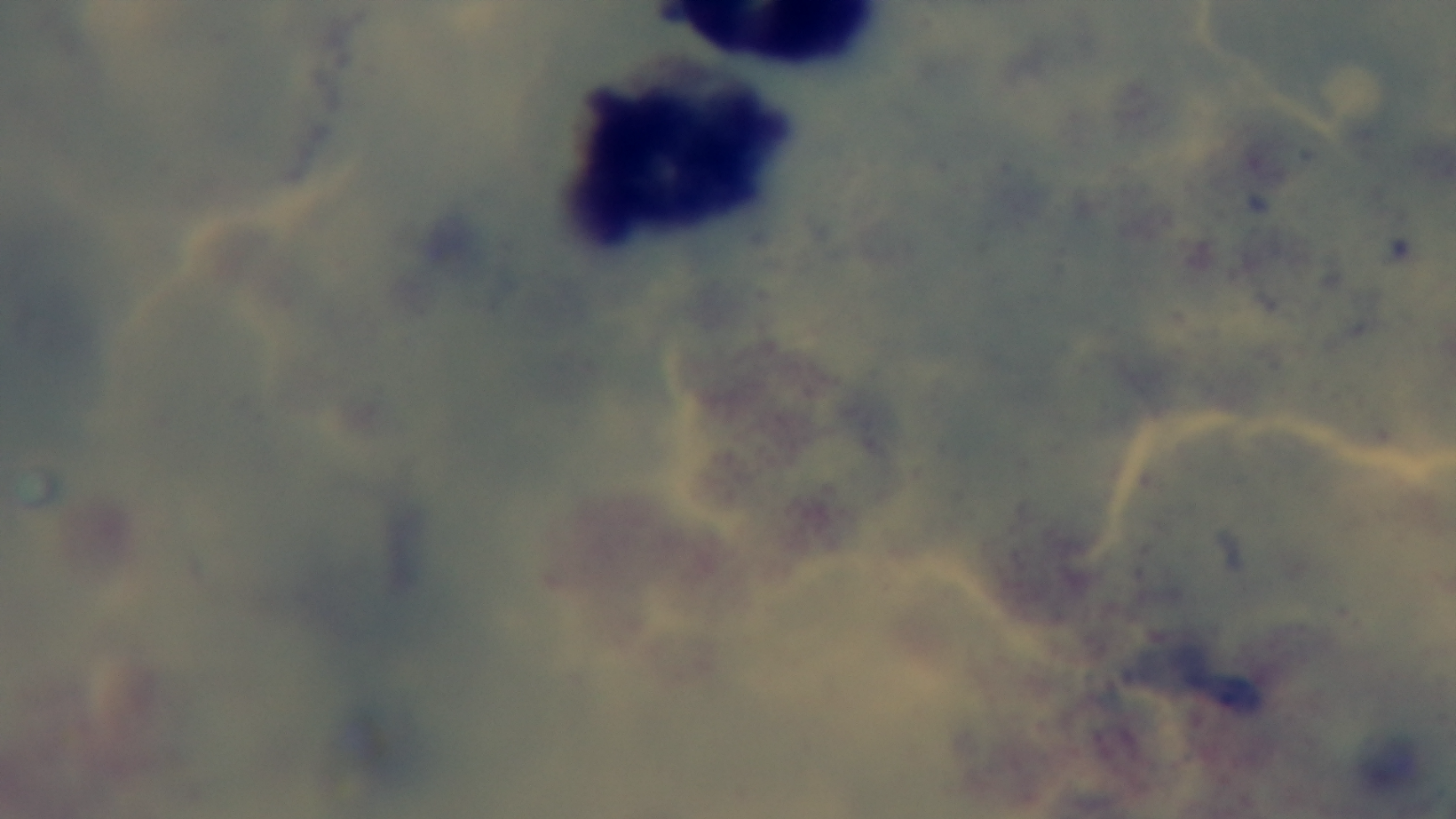
Summary:
  - Capture: mounted 4K digital camera
  - Stain: Giemsa
  - Preparation: thick smear
  - Malaria status: uninfected
  - Modality: light microscopy
  - Objective: 100x oil immersion
  - Field of view: one from the slide